Locate leukocytes (white blood cells).
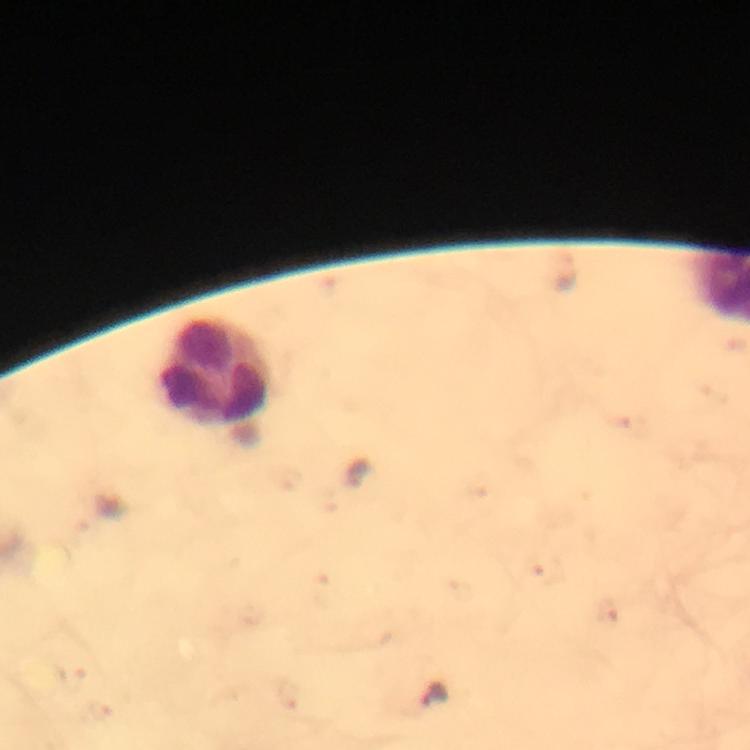
Approximate centers as [x, y] in pixels.
Leukocytes: [214, 374].

Summary:
  - Plasmodium parasite locations: [434, 694]
  - Stain: Giemsa
  - Magnification: 100x
  - Cropped from: a single field of view
  - Image size: 750×750 pixels
  - Preparation: thick blood smear
  - Capture: smartphone camera through the microscope
  - Immersion oil: applied
  - Context: from a malaria diagnostic workup